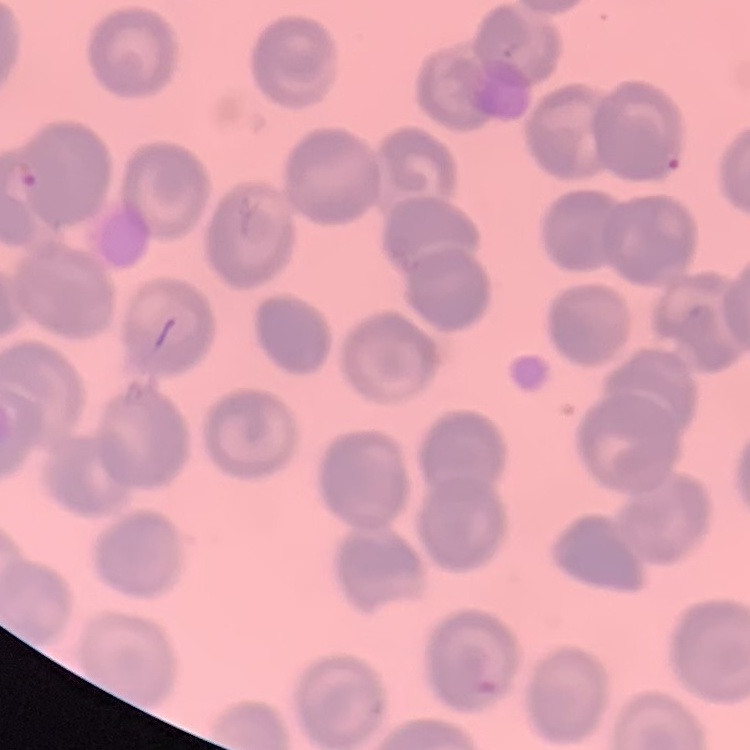
The red blood cells show no rouleaux formation. Thin blood film. Square crop of a larger photomicrograph. Stained with either Field's or Giemsa.